Report the malaria status of this cell.
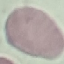
It is uninfected.

Giemsa-stained preparation. Automatically extracted cell patch, resized to 64 × 64 pixels. Thin smear of blood. Photographed with a smartphone camera at the microscope eyepiece.